Assess this cell for malaria.
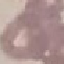

Uninfected.

Summary:
  - Image type: automatically extracted cell patch, resized to 64 × 64 pixels
  - Stain: Giemsa
  - Capture: smartphone through the microscope eyepiece
  - Preparation: thin smear